Classify this cell by malaria status.
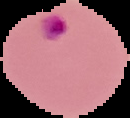

It is parasitized.

Summary:
  - Preparation: thin blood film
  - Image size: 130×118 pixels
  - Image type: segmented cell region on a black background